Identify the cell.
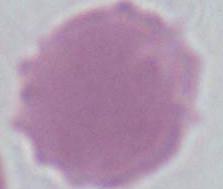
This is an erythrocyte.

Summary:
  - Magnification: 1000x
  - Modality: micrograph